Classify this cell by malaria status.
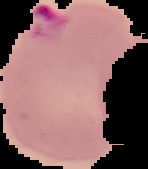
Parasitized.

image_size: 148×169 pixels
image_type: segmented cell region on a black background
preparation: thin blood film